Describe the morphology of the red blood cells.
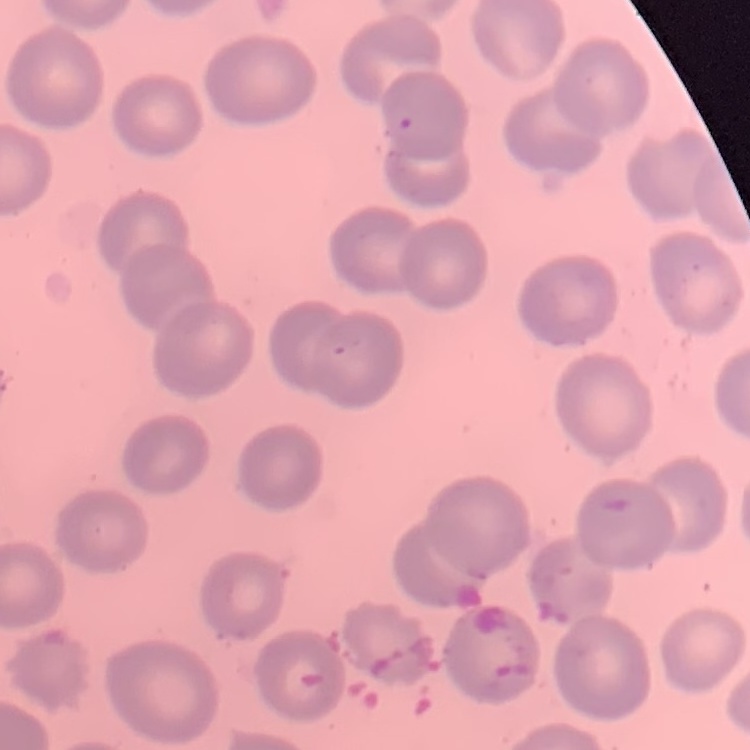
They show no rouleaux formation.

preparation: thin blood film
image_type: one tile cut from a larger photomicrograph
stain: Field's or Giemsa